Comment on the morphology of the red blood cells.
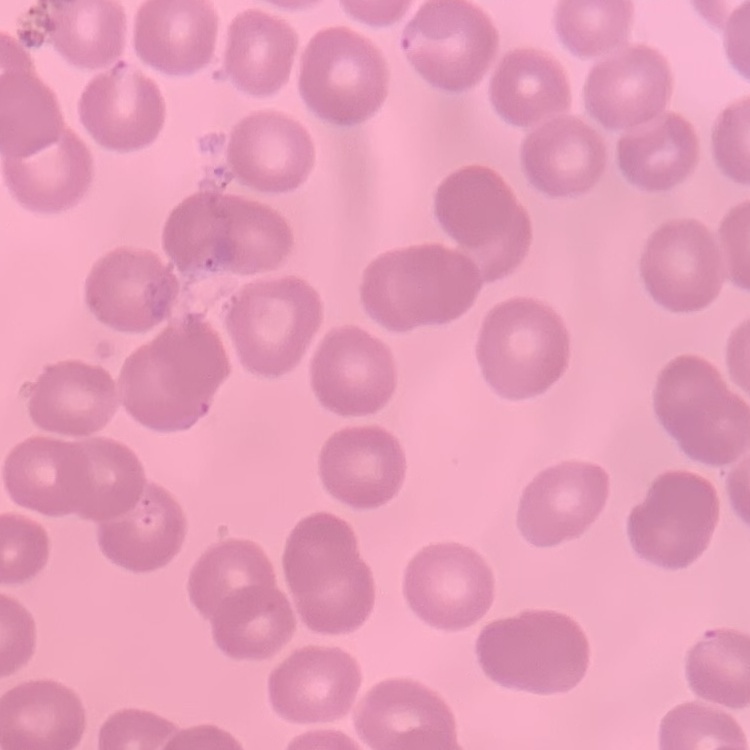

No rouleaux formation.

stain = Field's or Giemsa
image type = one tile cut from a larger photomicrograph
preparation = thin blood film